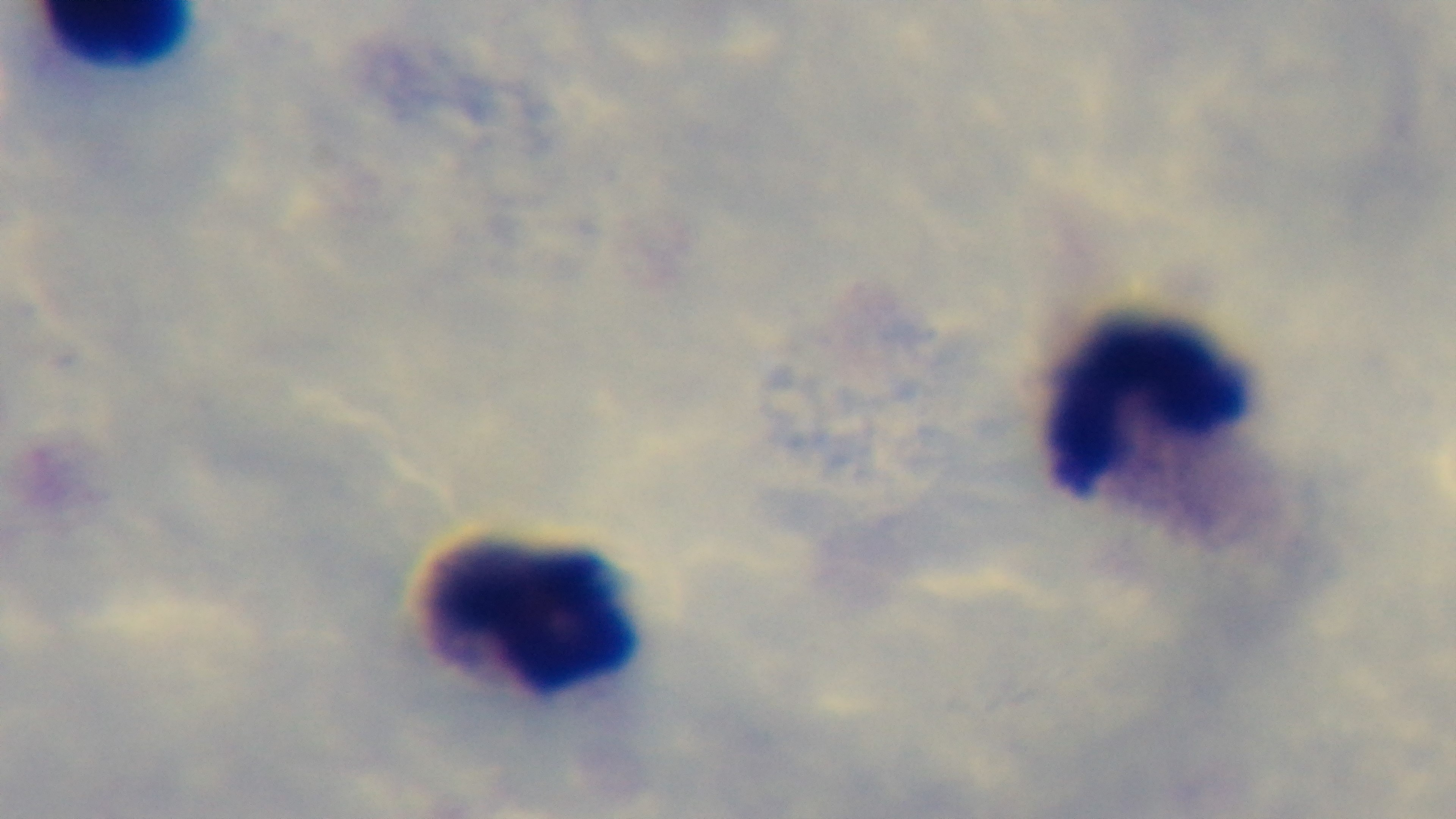 Malaria status: uninfected. Photomicrograph. Oil-immersion objective, 100x. Mounted 4K digital camera. One field from the slide. Giemsa-stained. Preparation: thick.